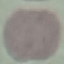

Summary:
  - Result: no malaria parasites seen
  - Preparation: thin smear
  - Image type: automatically extracted cell patch, resized to 64 × 64 pixels
  - Stain: Giemsa
  - Capture: smartphone camera at the microscope eyepiece